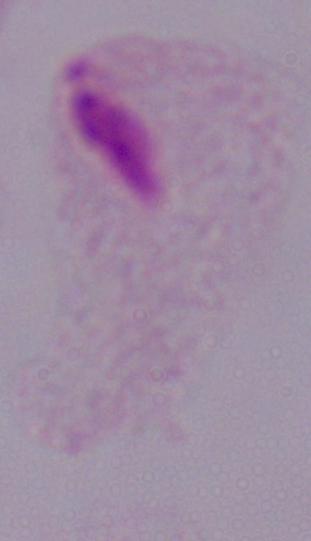

Summary:
  - Modality: micrograph
  - Magnification: 1000x
  - Identification: trichomonad